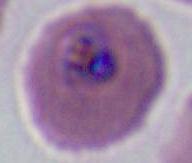

Captured at either 400x or 1000x magnification. Micrograph. A Plasmodium parasite is seen.